Report the malaria status of this cell.
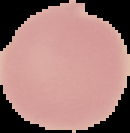
It is uninfected.

preparation = thin blood smear
image size = 130×133 pixels
image type = cell region segmented out of the field of view; surrounding area masked to black